State which cell type is depicted.
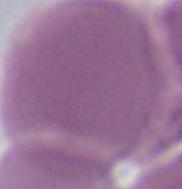
An erythrocyte.

magnification: 1000x
modality: micrograph